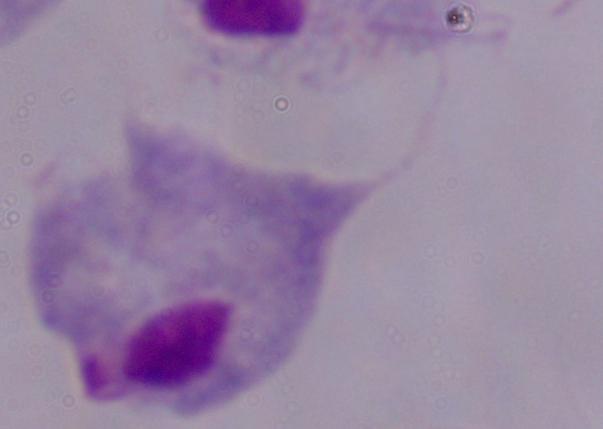
modality = photomicrograph
magnification = 1000x
identification = trichomonad